Point out each malaria parasite and each leukocyte.
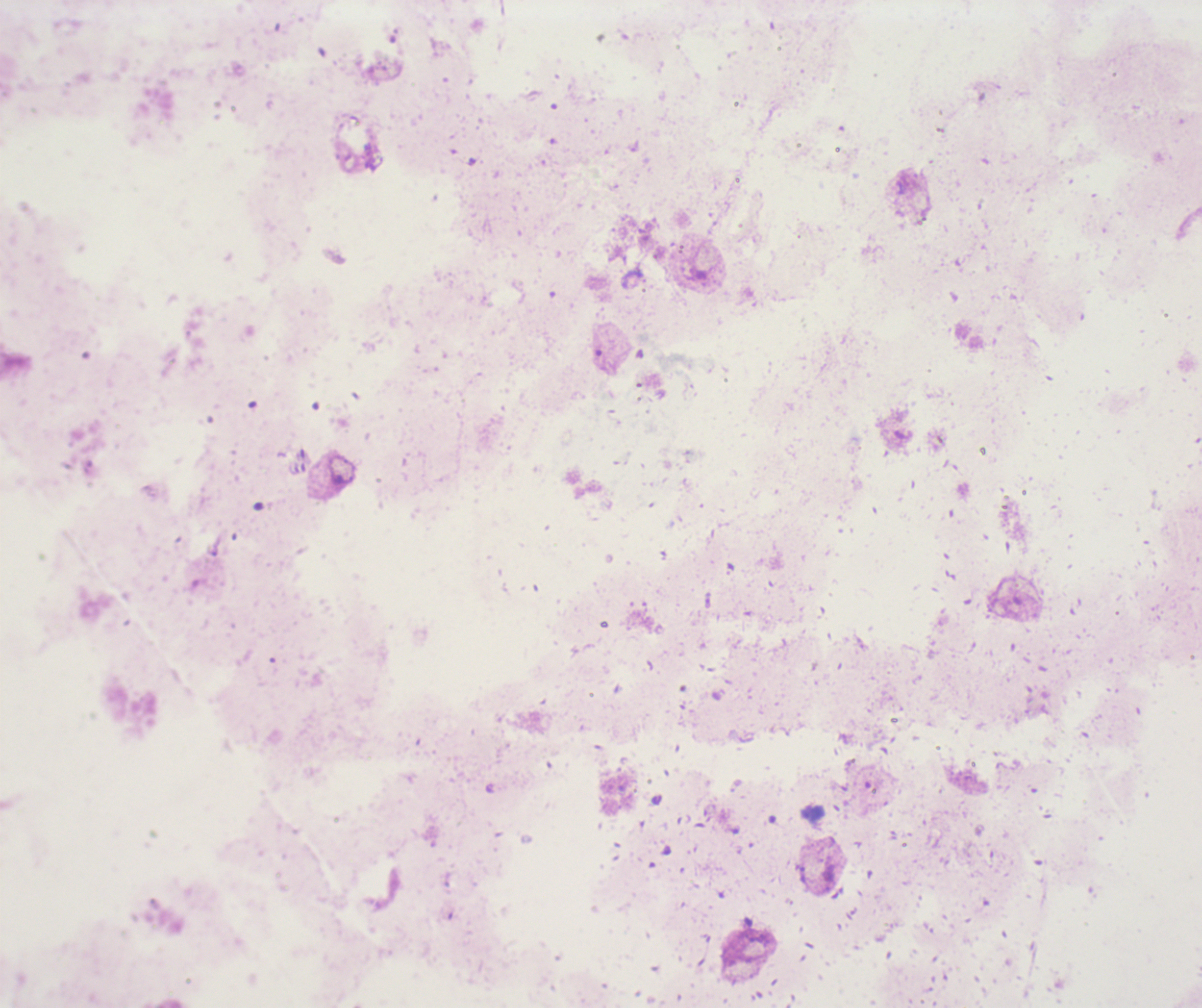
No malaria parasites seen.
No leukocytes visible.

Summary:
  - Background quality: poor
  - Field of view: single
  - Image size: 1202×1008 pixels
  - Coloration quality: bad
  - Preparation: thick smear of blood
  - Stain: Romanowsky
  - Context: previously used in an actual diagnosis
  - Magnification: 100x